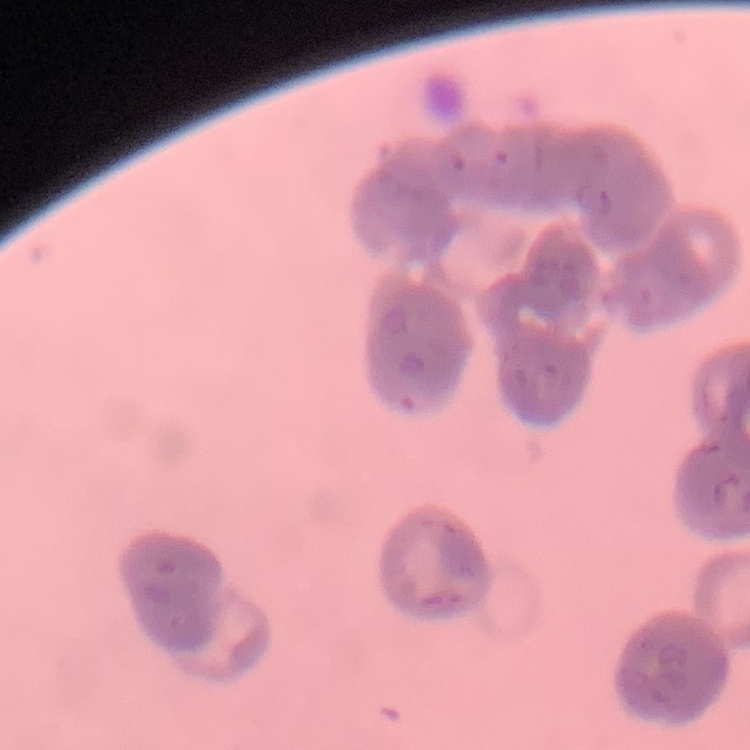
The erythrocytes show rouleaux formation. Field's or Giemsa stain. Thin peripheral smear. Square crop of a larger photomicrograph.